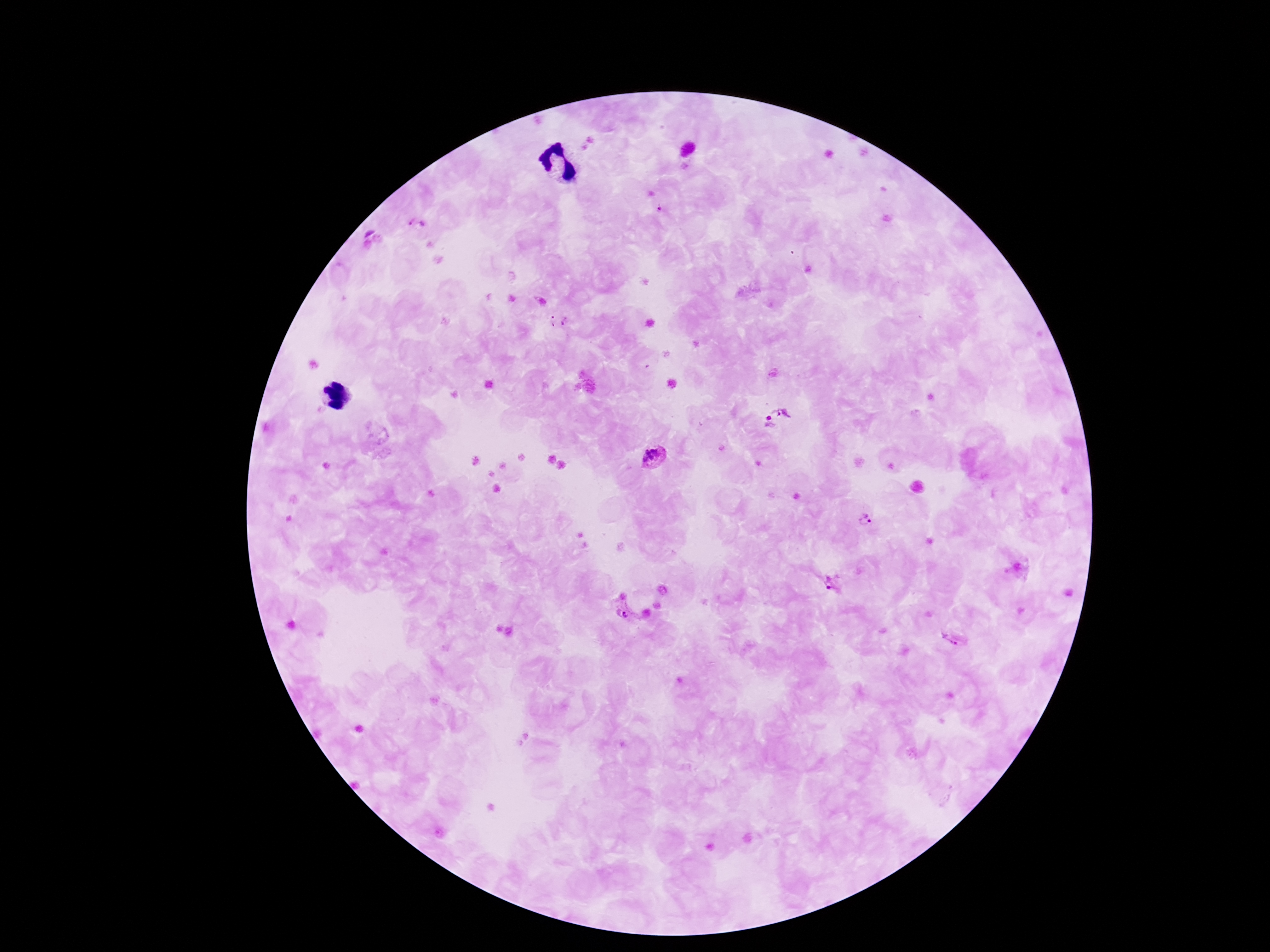
stain = Giemsa
Plasmodium parasite locations = approximate centers as [x, y] in pixels: [660, 207], [415, 222], [560, 320], [784, 406], [769, 424], [653, 457], [868, 514], [837, 585], [621, 612], [951, 638]
magnification = 100x
image size = 1270×952 pixels
patient malaria status = infected
preparation = thick peripheral-blood smear
capture = smartphone camera through the microscope eyepiece
field of view = one from this slide